Report the malaria status of this cell.
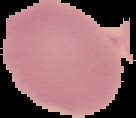
It is uninfected.

Cell region segmented out of the field of view; the surrounding area is masked to black. Image is 136×118 pixels. From a thin blood film.